Comment on the morphology of the erythrocytes.
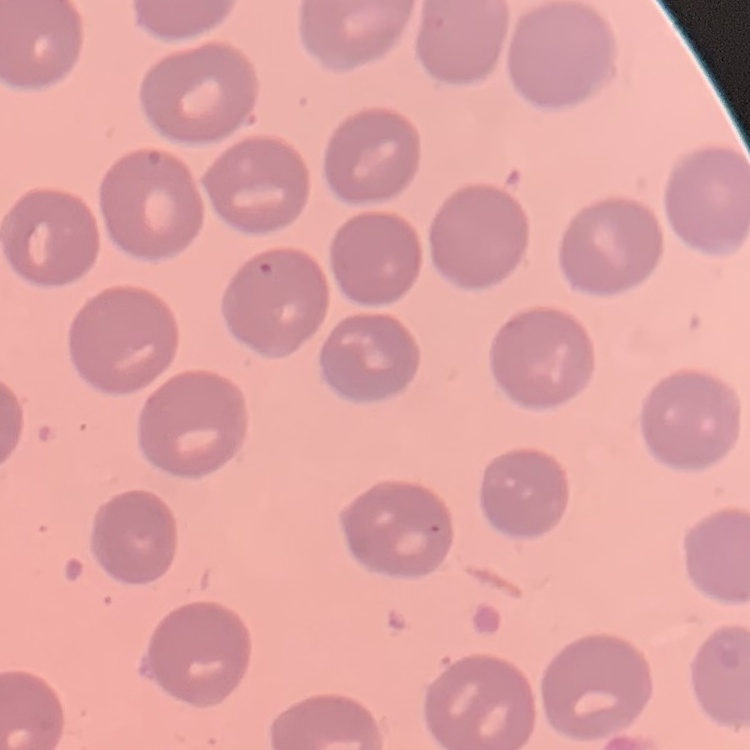

They show no rouleaux formation.

stain = Field's or Giemsa
image type = one tile cut from a larger photomicrograph
preparation = thin blood film